Comment on the morphology of the erythrocytes.
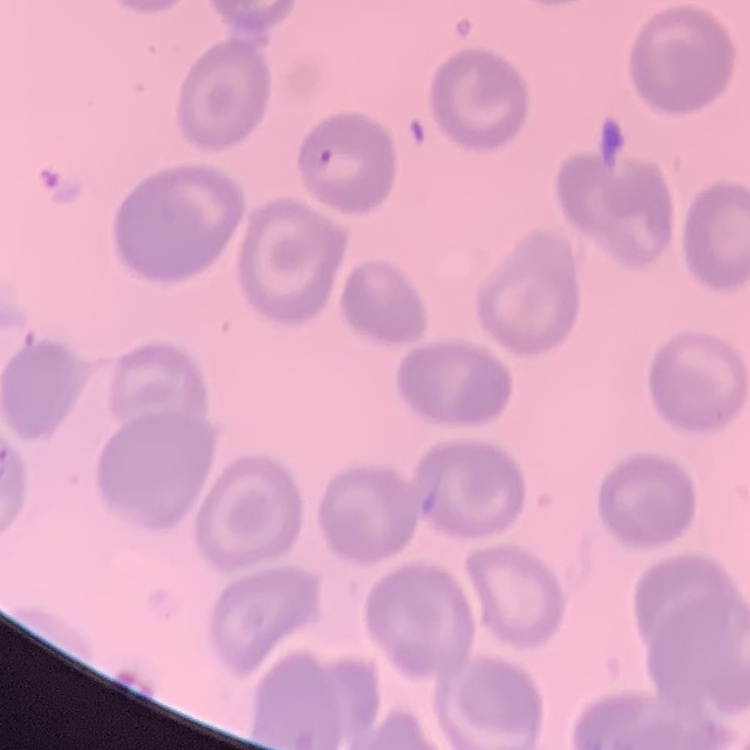
They show no rouleaux formation.

Field's or Giemsa stain. One tile cut from a larger photomicrograph. Thin peripheral smear.